Classify this cell by malaria status.
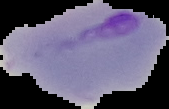
Parasitized.

Summary:
  - Image type: segmented cell region on a black background
  - Preparation: thin blood smear
  - Image size: 169×109 pixels